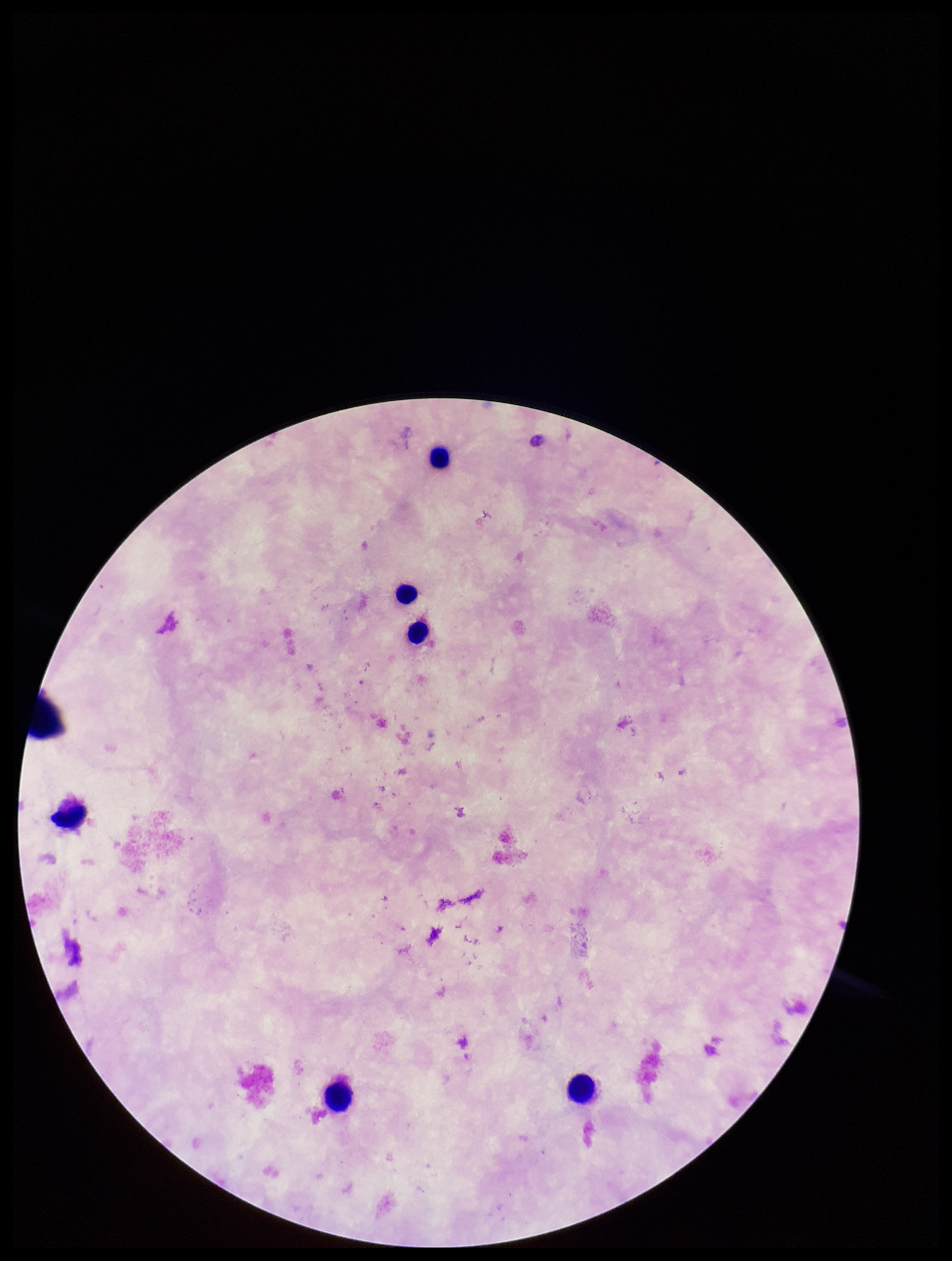
Summary:
  - Parasite count: 0
  - Preparation: thick smear
  - Stain: Giemsa
  - Image size: 952×1261 pixels
  - Patient malaria status: negative
  - Leukocyte count: 6
  - Capture: smartphone photograph through the microscope eyepiece
  - Field of view: one from this slide
  - Plasmodium parasites: none seen